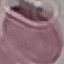 Malaria status: uninfected. Acquired by smartphone through the microscope eyepiece. Automatically extracted cell patch, resized to 64 × 64 pixels. Thin blood film. Giemsa-stained preparation.